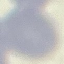
Result: no malaria parasites seen. Automatically extracted cell patch, resized to 64 × 64 pixels. Thin smear of blood. Acquired by smartphone through the microscope eyepiece. Giemsa-stained preparation.